Name the parasite shown.
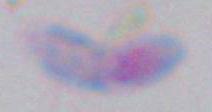

Toxoplasma gondii.

Summary:
  - Magnification: 1000x
  - Modality: photomicrograph